Report the malaria status of this cell.
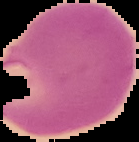

Parasitized.

Summary:
  - Image type: segmented cell region with the area outside set to black
  - Preparation: thin blood film
  - Image size: 139×142 pixels